Assess the morphology of the erythrocytes.
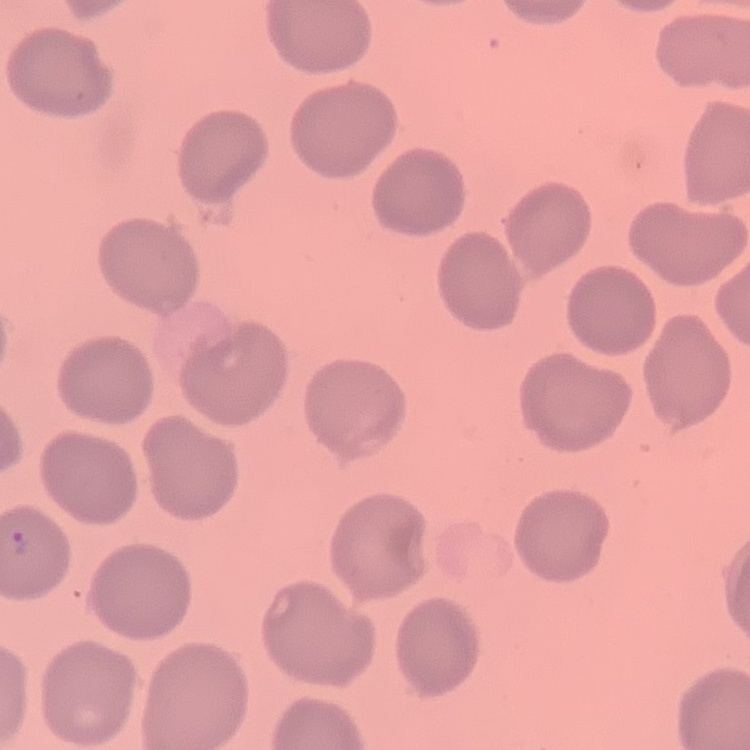

No rouleaux formation.

Thin blood smear. Square crop of a larger photomicrograph. Field's or Giemsa stain.